Comment on the morphology of the red blood cells.
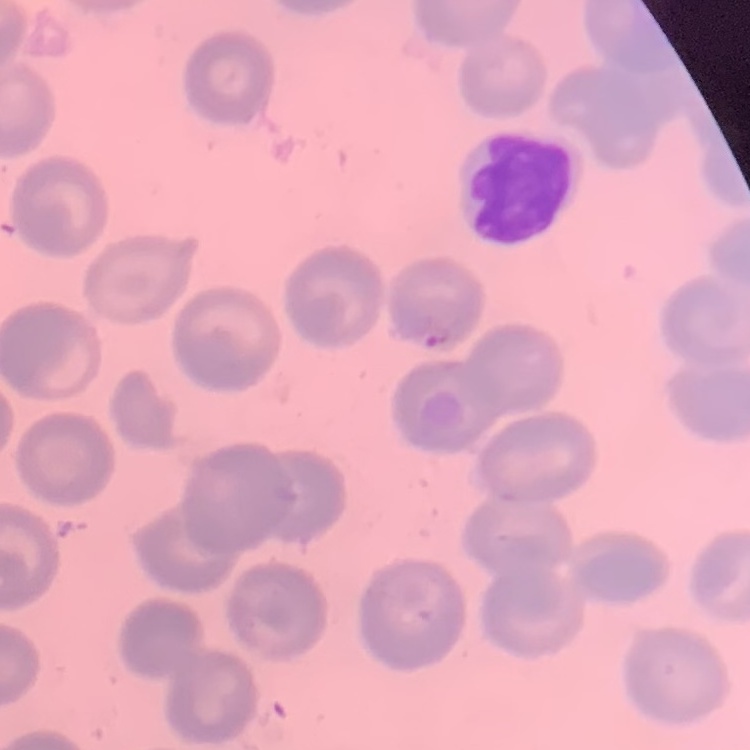

No rouleaux formation.

Field's or Giemsa stain. Thin blood film. Square crop of a larger photomicrograph.